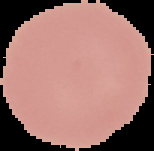
From a thin blood smear. Result: negative for malaria parasites. The area outside the segmented cell region is set to black. Image is 154×151 pixels.